Locate and identify every blood parasite.
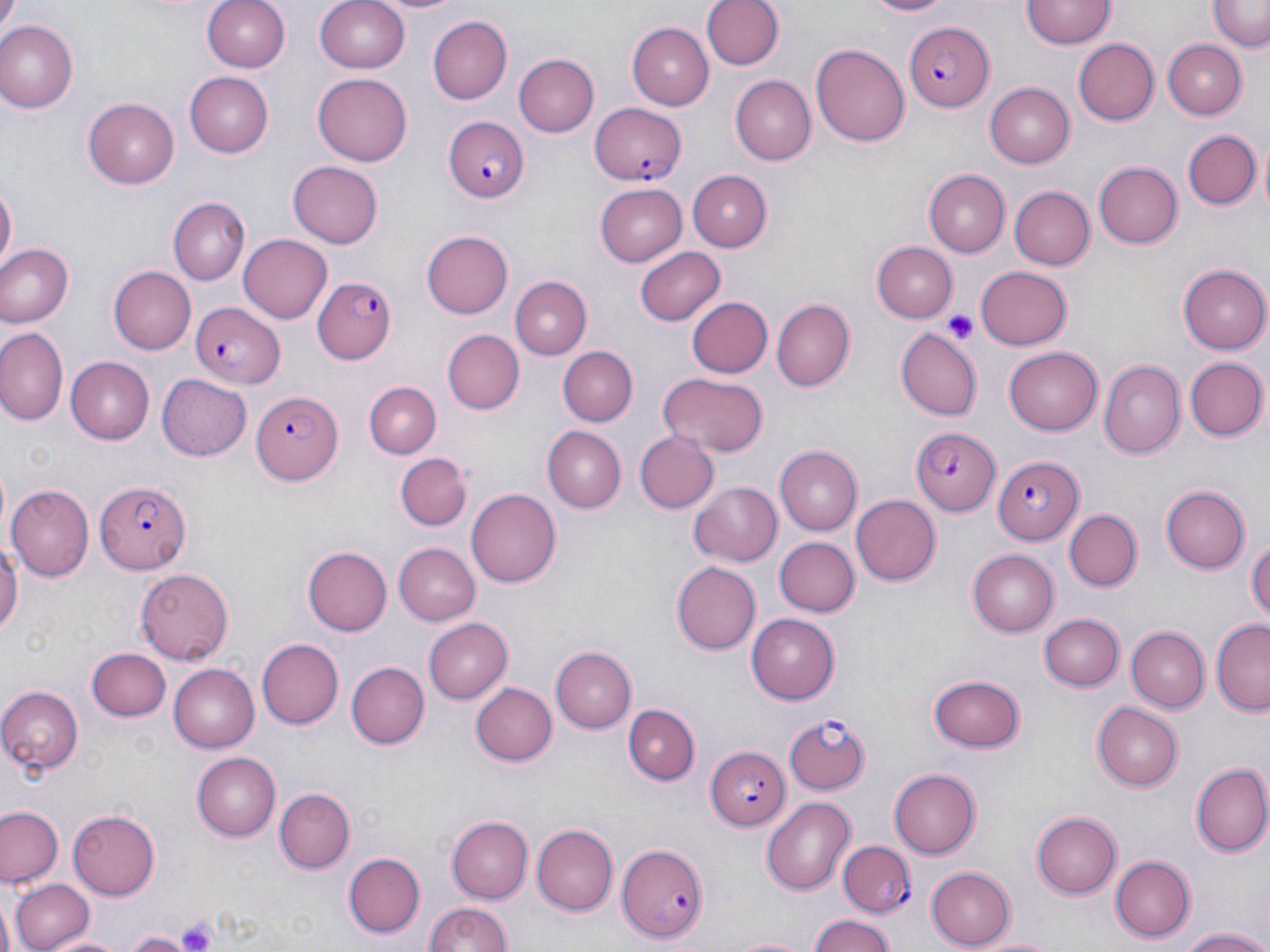
Approximate bounding boxes as [x1, y1, x2, y2] in pixels.
Plasmodium falciparum-infected red blood cells: [902, 21, 992, 110], [589, 102, 687, 186], [444, 116, 529, 202], [313, 275, 397, 365], [189, 301, 283, 385], [250, 390, 340, 486], [911, 424, 1000, 518], [993, 455, 1084, 543], [94, 479, 189, 574], [782, 714, 870, 796], [706, 747, 790, 828], [614, 841, 709, 942], [840, 841, 915, 916].
No Plasmodium ovale, Plasmodium malariae, Plasmodium vivax, Babesia divergens, or Trypanosoma brucei observed.

Summary:
  - Uninfected red blood cell locations: [202, 0, 290, 72], [314, 0, 412, 73], [374, 0, 466, 15], [700, 0, 781, 71], [861, 0, 958, 19], [1023, 0, 1115, 48], [1207, 3, 1269, 51], [426, 14, 511, 102], [2, 22, 78, 112], [628, 23, 714, 109], [1073, 39, 1158, 126], [1163, 39, 1247, 119], [811, 45, 910, 146], [514, 54, 600, 137], [184, 72, 273, 156], [314, 72, 413, 165], [729, 75, 814, 165], [985, 83, 1075, 167], [83, 97, 179, 189], [1182, 131, 1260, 210], [1092, 161, 1183, 250], [288, 162, 383, 248], [921, 169, 1008, 258], [687, 170, 771, 250], [594, 182, 687, 264], [1, 185, 16, 275], [1011, 186, 1095, 270], [169, 197, 250, 286], [421, 230, 513, 319], [238, 234, 333, 324], [870, 241, 956, 323], [2, 244, 74, 327], [636, 247, 725, 327], [651, 257, 766, 349], [1182, 262, 1270, 354], [107, 265, 195, 354], [977, 265, 1073, 348], [509, 276, 590, 360], [687, 297, 772, 378], [772, 298, 855, 389], [0, 327, 66, 425], [899, 327, 982, 420], [442, 329, 523, 414], [1004, 346, 1102, 436], [557, 347, 638, 426], [66, 356, 154, 445], [1185, 358, 1267, 442], [1100, 361, 1186, 458], [156, 373, 251, 460], [658, 373, 768, 457], [364, 382, 442, 458], [541, 426, 625, 514], [633, 430, 718, 514], [774, 446, 863, 535], [396, 452, 472, 530], [690, 480, 782, 564], [9, 484, 95, 581], [1159, 484, 1249, 575], [467, 488, 561, 588], [852, 494, 941, 585], [1063, 509, 1143, 592], [0, 526, 21, 642], [1247, 535, 1270, 631], [774, 536, 859, 617], [393, 542, 480, 623], [304, 545, 394, 636], [967, 548, 1061, 635], [674, 560, 761, 655], [134, 568, 234, 664], [746, 612, 839, 705], [1040, 613, 1124, 692], [422, 616, 512, 704], [1212, 621, 1270, 716], [1125, 626, 1209, 712], [256, 639, 343, 728], [552, 646, 635, 733], [89, 647, 170, 722], [345, 660, 430, 749], [167, 663, 259, 751], [930, 671, 1026, 749], [469, 682, 557, 766], [0, 686, 86, 772], [1091, 701, 1183, 790], [623, 703, 699, 783], [192, 753, 279, 841], [1191, 763, 1270, 856], [888, 768, 982, 858], [275, 788, 354, 873], [762, 796, 858, 896], [0, 805, 64, 886], [68, 809, 163, 899], [1030, 812, 1121, 899], [446, 817, 531, 901], [532, 824, 617, 915], [432, 835, 523, 943], [344, 853, 424, 938], [1109, 854, 1195, 942], [925, 866, 1017, 948], [11, 880, 95, 952], [423, 900, 512, 952], [806, 913, 899, 952], [1179, 927, 1270, 952], [123, 932, 191, 952], [977, 932, 1058, 952], [46, 934, 129, 952], [726, 934, 818, 952]
  - Platelet locations: [941, 308, 979, 343], [178, 918, 216, 952]
  - Slide-level diagnosis: Plasmodium falciparum
  - Image size: 1270×952 pixels
  - Field of view: single
  - Magnification: 1000x
  - Preparation: thin blood film
  - Modality: optical microscopy
  - Stain: May-Grünwald-Giemsa